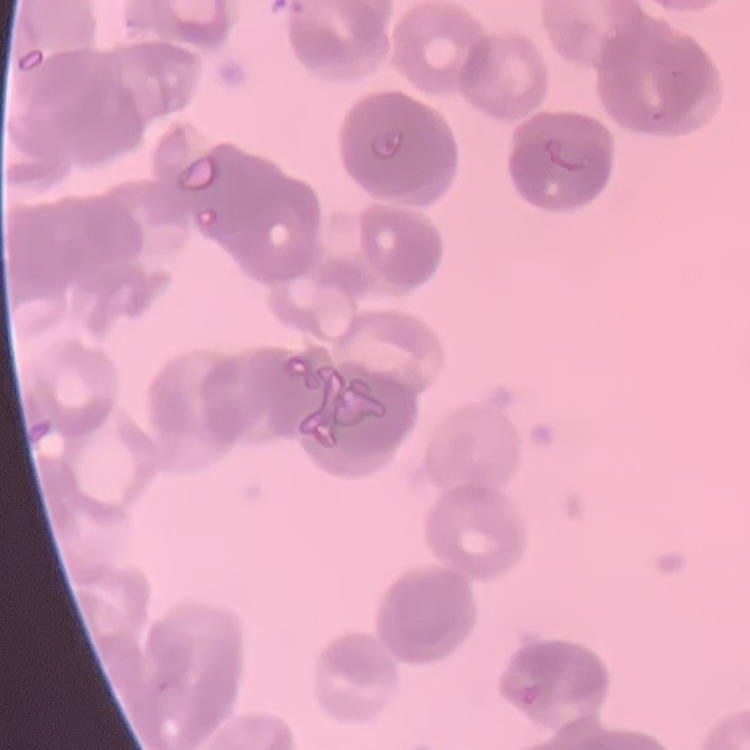

Summary:
  - Erythrocyte morphology: rouleaux formation
  - Stain: Field's or Giemsa
  - Image type: one tile cut from a larger photomicrograph
  - Preparation: thin blood film